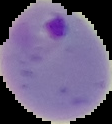 Malaria status: parasitized. Cell region segmented out of the field of view; the surrounding area is masked to black. From a thin blood film. Image is 112×124 pixels.